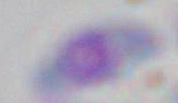

modality = photomicrograph
identification = Toxoplasma gondii
magnification = 1000x